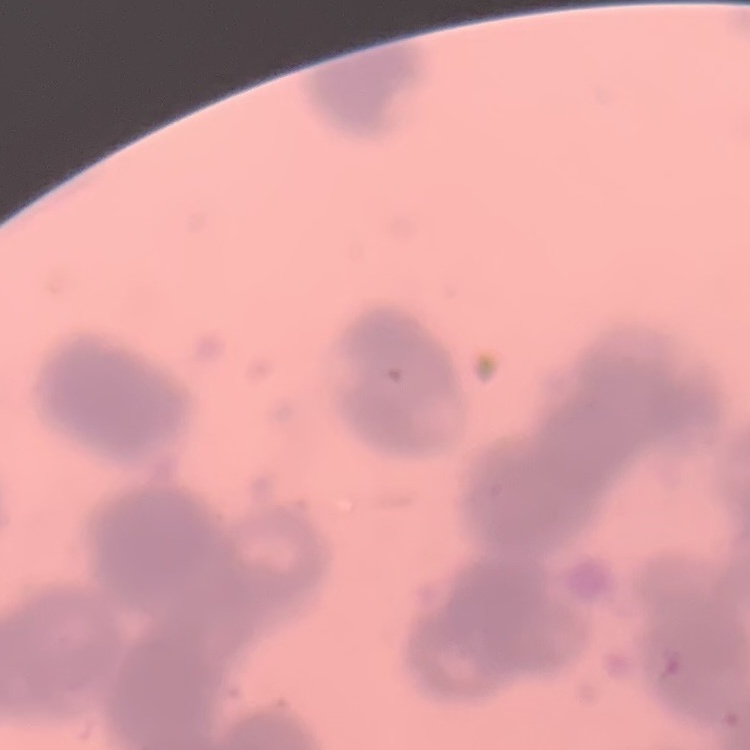

The red blood cells show rouleaux formation. Thin blood smear. One tile cut from a larger photomicrograph. Stained with either Field's or Giemsa.